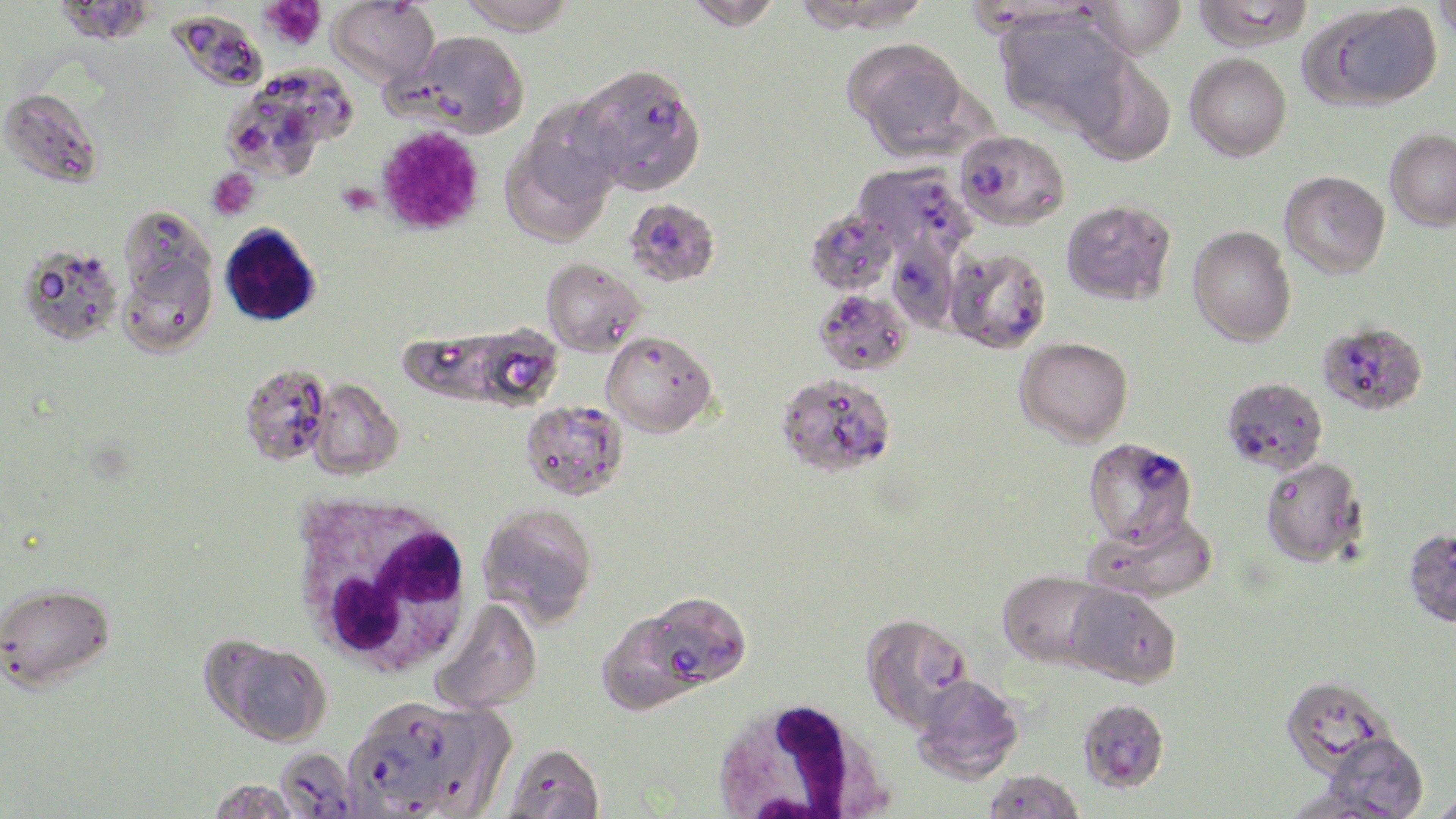

slide-level diagnosis = Plasmodium falciparum
image size = 1456×819 pixels
platelet locations = approximate bounding boxes as named x1/y1/x2/y2 corners in pixels: (x1=260, y1=0, x2=327, y2=50), (x1=375, y1=126, x2=485, y2=238), (x1=206, y1=168, x2=260, y2=221), (x1=336, y1=180, x2=380, y2=216)
white blood cell locations = approximate bounding boxes as named x1/y1/x2/y2 corners in pixels: (x1=288, y1=488, x2=476, y2=678), (x1=708, y1=696, x2=894, y2=818)
uninfected red blood cell locations = approximate bounding boxes as named x1/y1/x2/y2 corners in pixels: (x1=54, y1=0, x2=158, y2=46), (x1=455, y1=0, x2=575, y2=35), (x1=683, y1=0, x2=783, y2=30), (x1=792, y1=0, x2=933, y2=36), (x1=1080, y1=0, x2=1187, y2=59), (x1=1192, y1=0, x2=1312, y2=52), (x1=1432, y1=0, x2=1456, y2=46), (x1=329, y1=1, x2=439, y2=88), (x1=1309, y1=3, x2=1442, y2=109), (x1=995, y1=11, x2=1132, y2=138), (x1=168, y1=16, x2=270, y2=91), (x1=405, y1=30, x2=529, y2=138), (x1=846, y1=40, x2=971, y2=155), (x1=1184, y1=52, x2=1291, y2=161), (x1=1071, y1=55, x2=1176, y2=166), (x1=223, y1=67, x2=352, y2=181), (x1=0, y1=87, x2=102, y2=187), (x1=1385, y1=129, x2=1456, y2=230), (x1=501, y1=133, x2=616, y2=246), (x1=1279, y1=170, x2=1390, y2=278), (x1=1060, y1=199, x2=1176, y2=305), (x1=117, y1=208, x2=219, y2=349), (x1=219, y1=223, x2=321, y2=327), (x1=1187, y1=226, x2=1296, y2=346), (x1=17, y1=243, x2=123, y2=346), (x1=541, y1=258, x2=647, y2=356), (x1=814, y1=288, x2=913, y2=375), (x1=396, y1=325, x2=553, y2=408), (x1=601, y1=330, x2=718, y2=437), (x1=1015, y1=336, x2=1133, y2=446), (x1=239, y1=363, x2=333, y2=467), (x1=308, y1=378, x2=404, y2=479), (x1=1260, y1=456, x2=1366, y2=567), (x1=477, y1=503, x2=598, y2=626), (x1=1083, y1=509, x2=1218, y2=604), (x1=1403, y1=526, x2=1456, y2=627), (x1=997, y1=569, x2=1113, y2=669), (x1=1064, y1=582, x2=1181, y2=688), (x1=431, y1=599, x2=543, y2=715), (x1=601, y1=616, x2=703, y2=712), (x1=208, y1=637, x2=332, y2=745), (x1=1281, y1=673, x2=1396, y2=778), (x1=910, y1=674, x2=1024, y2=783), (x1=1323, y1=732, x2=1429, y2=818), (x1=204, y1=777, x2=306, y2=818), (x1=1429, y1=788, x2=1456, y2=819)
field of view = single
preparation = thin blood film
magnification = 1000x
Plasmodium falciparum-infected red blood cell locations = approximate bounding boxes as named x1/y1/x2/y2 corners in pixels: (x1=601, y1=88, x2=709, y2=191), (x1=955, y1=130, x2=1069, y2=230), (x1=854, y1=162, x2=978, y2=263), (x1=627, y1=198, x2=717, y2=287), (x1=805, y1=207, x2=899, y2=295), (x1=892, y1=242, x2=971, y2=328), (x1=945, y1=246, x2=1052, y2=354), (x1=1313, y1=320, x2=1427, y2=416), (x1=776, y1=373, x2=897, y2=477), (x1=1221, y1=377, x2=1328, y2=475), (x1=520, y1=400, x2=628, y2=501), (x1=1082, y1=436, x2=1197, y2=547), (x1=0, y1=580, x2=114, y2=690), (x1=651, y1=591, x2=751, y2=683), (x1=860, y1=613, x2=973, y2=730), (x1=1077, y1=698, x2=1170, y2=792), (x1=371, y1=700, x2=477, y2=786), (x1=344, y1=728, x2=436, y2=816), (x1=502, y1=742, x2=605, y2=818), (x1=273, y1=747, x2=361, y2=817), (x1=982, y1=769, x2=1084, y2=818)
modality = light microscopy
stain = May-Grünwald-Giemsa